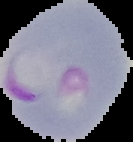
image type = segmented cell region with the area outside set to black
malaria status = parasitized
image size = 133×142 pixels
preparation = thin blood film